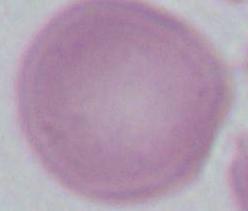

Captured at 1000x magnification. An erythrocyte is seen. Micrograph.